State the blood parasite species.
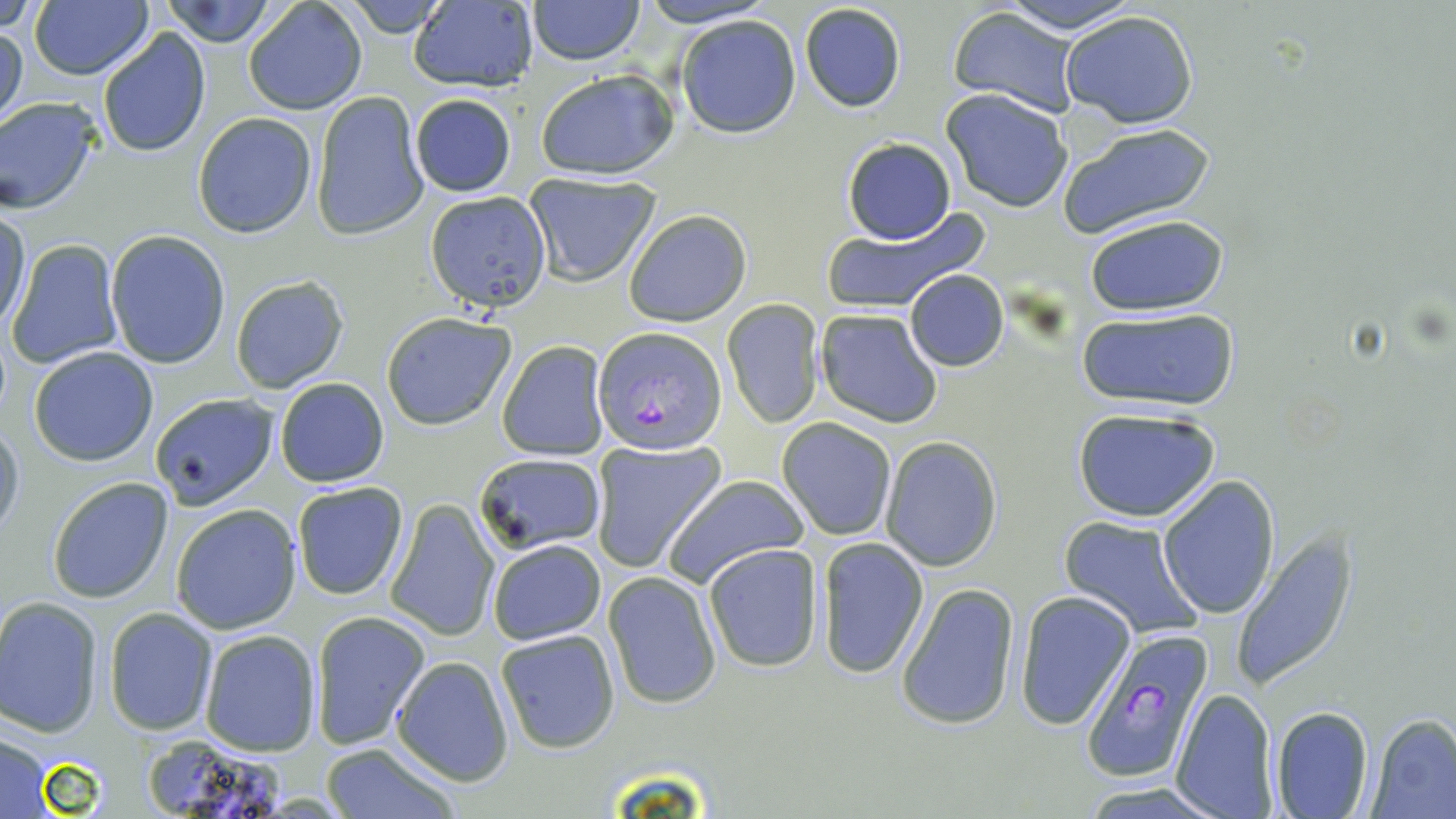
Plasmodium falciparum.

Approximate bounding boxes as named x1/y1/x2/y2 corners in pixels. Plasmodium falciparum-infected red blood cell locations: (x1=592, y1=327, x2=726, y2=456), (x1=1080, y1=633, x2=1215, y2=783). Uninfected red blood cell locations: (x1=0, y1=0, x2=50, y2=32), (x1=161, y1=0, x2=281, y2=47), (x1=339, y1=0, x2=452, y2=35), (x1=526, y1=0, x2=645, y2=65), (x1=634, y1=0, x2=780, y2=27), (x1=995, y1=0, x2=1144, y2=33), (x1=243, y1=1, x2=368, y2=116), (x1=29, y1=2, x2=154, y2=81), (x1=407, y1=2, x2=535, y2=91), (x1=798, y1=3, x2=907, y2=114), (x1=946, y1=6, x2=1085, y2=116), (x1=1061, y1=9, x2=1198, y2=128), (x1=675, y1=15, x2=801, y2=139), (x1=0, y1=20, x2=26, y2=133), (x1=97, y1=28, x2=210, y2=157), (x1=534, y1=69, x2=678, y2=180), (x1=941, y1=90, x2=1074, y2=213), (x1=310, y1=91, x2=429, y2=241), (x1=407, y1=92, x2=517, y2=198), (x1=0, y1=97, x2=103, y2=213), (x1=193, y1=112, x2=318, y2=239), (x1=1057, y1=122, x2=1216, y2=239), (x1=841, y1=136, x2=956, y2=244), (x1=522, y1=172, x2=662, y2=285), (x1=426, y1=189, x2=554, y2=335), (x1=818, y1=206, x2=987, y2=316), (x1=2, y1=209, x2=32, y2=331), (x1=622, y1=209, x2=753, y2=327), (x1=1082, y1=215, x2=1230, y2=315), (x1=105, y1=229, x2=231, y2=369), (x1=6, y1=239, x2=124, y2=369), (x1=904, y1=269, x2=1009, y2=370), (x1=230, y1=273, x2=350, y2=394), (x1=723, y1=300, x2=825, y2=427), (x1=815, y1=308, x2=943, y2=428), (x1=1072, y1=308, x2=1242, y2=415), (x1=380, y1=312, x2=516, y2=430), (x1=496, y1=341, x2=609, y2=460), (x1=26, y1=346, x2=159, y2=467), (x1=275, y1=377, x2=388, y2=488), (x1=148, y1=392, x2=279, y2=509), (x1=1073, y1=406, x2=1221, y2=523), (x1=0, y1=417, x2=24, y2=545), (x1=775, y1=417, x2=897, y2=540), (x1=880, y1=437, x2=1003, y2=571), (x1=590, y1=439, x2=726, y2=573), (x1=475, y1=452, x2=607, y2=555), (x1=660, y1=473, x2=812, y2=590), (x1=1158, y1=474, x2=1280, y2=618), (x1=47, y1=475, x2=175, y2=604), (x1=291, y1=481, x2=409, y2=600), (x1=385, y1=498, x2=499, y2=642), (x1=171, y1=504, x2=302, y2=635), (x1=1060, y1=516, x2=1204, y2=639), (x1=1231, y1=530, x2=1359, y2=692), (x1=815, y1=536, x2=931, y2=679), (x1=485, y1=538, x2=609, y2=644), (x1=703, y1=543, x2=826, y2=673), (x1=603, y1=570, x2=722, y2=709), (x1=895, y1=580, x2=1021, y2=731), (x1=1015, y1=590, x2=1136, y2=729), (x1=0, y1=597, x2=103, y2=736), (x1=105, y1=607, x2=217, y2=735), (x1=310, y1=609, x2=429, y2=751), (x1=199, y1=629, x2=322, y2=756), (x1=495, y1=629, x2=621, y2=753), (x1=390, y1=655, x2=514, y2=787), (x1=1170, y1=687, x2=1281, y2=818), (x1=1270, y1=704, x2=1374, y2=818), (x1=1367, y1=713, x2=1456, y2=818), (x1=0, y1=732, x2=56, y2=816), (x1=138, y1=735, x2=294, y2=819), (x1=318, y1=743, x2=460, y2=819), (x1=1078, y1=783, x2=1230, y2=818). Image is 1456×819 pixels. May-Grünwald-Giemsa-stained preparation. Optical microscopy. Thin blood smear. One field of a larger specimen. 1000x magnification.